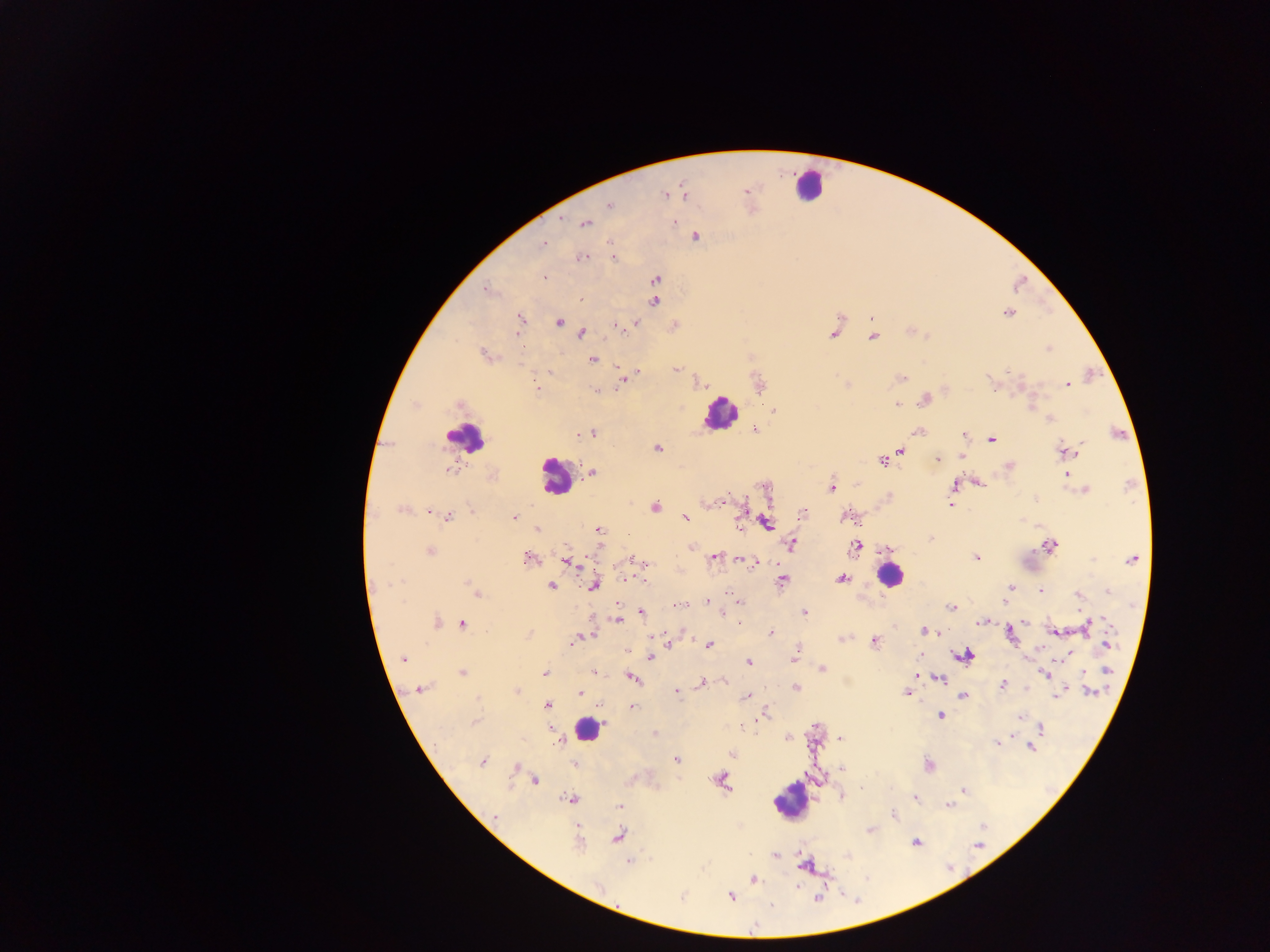

Approximate centers as {x, y} in pixels.
Summary:
  - Leukocyte locations: {809, 185}, {719, 413}, {464, 438}, {555, 475}, {889, 576}, {587, 728}, {789, 802}
  - Malaria parasite locations: {745, 191}, {684, 193}, {664, 195}, {609, 205}, {674, 222}, {585, 223}, {696, 237}, {610, 243}, {543, 245}, {613, 257}, {581, 259}, {544, 277}, {656, 278}, {486, 290}, {581, 299}, {654, 301}, {1009, 313}, {519, 318}, {871, 318}, {559, 322}, {635, 323}, {618, 327}, {581, 333}, {833, 334}, {874, 336}, {1048, 349}, {484, 354}, {592, 359}, {616, 368}, {676, 369}, {638, 372}, {902, 378}, {621, 380}, {1068, 385}, {537, 388}, {597, 390}, {925, 400}, {897, 404}, {458, 405}, {773, 410}, {1049, 420}, {754, 429}, {919, 431}, {592, 434}, {577, 435}, {963, 435}, {991, 439}, {657, 448}, {901, 450}, {1064, 451}, {1077, 452}, {962, 456}, {882, 460}, {938, 460}, {1009, 467}, {447, 469}, {591, 472}, {1067, 474}, {979, 483}, {954, 486}, {830, 488}, {1084, 490}, {725, 498}, {1035, 498}, {951, 500}, {708, 503}, {950, 505}, {654, 507}, {401, 509}, {430, 511}, {471, 511}, {803, 514}, {684, 516}, {847, 516}, {448, 517}, {514, 517}, {766, 522}, {537, 530}, {598, 530}, {931, 539}, {792, 544}, {857, 546}, {1050, 546}, {691, 547}, {598, 549}, {886, 549}, {430, 552}, {715, 557}, {977, 557}, {528, 559}, {633, 560}, {1131, 560}, {567, 561}, {638, 561}, {751, 563}, {631, 578}, {841, 578}, {782, 580}, {471, 585}, {594, 585}, {551, 586}, {1011, 587}, {1041, 591}, {1107, 592}, {477, 593}, {1078, 596}, {707, 601}, {739, 602}, {1004, 602}, {680, 605}, {952, 607}, {642, 612}, {805, 612}, {723, 614}, {617, 620}, {982, 621}, {437, 622}, {1025, 622}, {463, 624}, {1087, 627}, {1055, 631}, {771, 632}, {924, 632}, {588, 636}, {1010, 636}, {577, 638}, {842, 638}, {573, 641}, {873, 641}, {709, 645}, {1108, 645}, {628, 650}, {796, 652}, {1069, 654}, {964, 656}, {651, 657}, {404, 659}, {749, 662}, {822, 668}, {1107, 670}, {594, 672}, {462, 673}, {544, 673}, {1045, 674}, {916, 676}, {633, 677}, {939, 679}, {725, 681}, {702, 682}, {1003, 685}, {796, 687}, {420, 689}, {516, 691}, {676, 692}, {1089, 692}, {580, 693}, {906, 693}, {746, 696}, {963, 696}, {1056, 696}, {600, 704}, {546, 705}, {632, 706}, {764, 715}, {940, 716}, {1021, 716}, {475, 721}, {741, 726}, {1042, 727}, {655, 733}, {788, 738}, {839, 739}, {560, 741}, {997, 744}, {1031, 747}, {732, 754}, {676, 760}, {482, 762}, {574, 764}, {929, 766}, {516, 767}, {536, 780}, {722, 781}, {862, 788}, {964, 791}, {842, 797}, {916, 798}, {570, 799}, {948, 805}, {620, 806}, {893, 813}, {495, 817}, {870, 830}, {617, 836}, {916, 842}, {578, 844}, {775, 856}, {629, 862}, {803, 865}, {754, 879}, {731, 896}, {818, 898}, {771, 905}, {754, 925}
  - Image size: 1270×952 pixels
  - Capture: mobile-phone photograph through a microscope
  - Preparation: thick blood film
  - Field of view: single
  - Country: Ghana